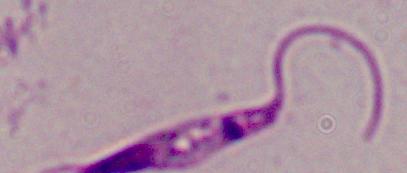 A Leishmania parasite is seen. 1000x magnification. Photomicrograph.